Comment on the morphology of the erythrocytes.
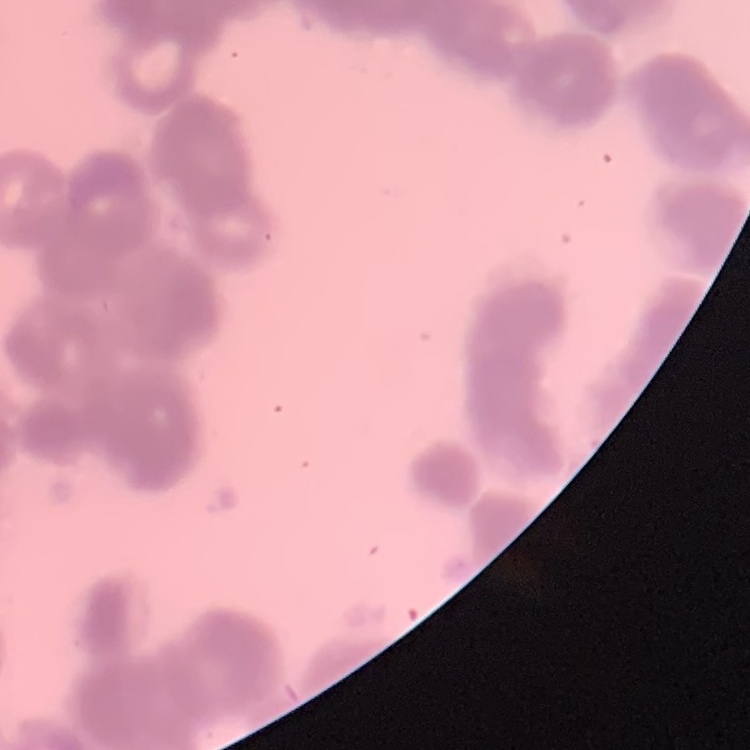

They show rouleaux formation.

preparation = thin blood film
image type = one tile cut from a larger photomicrograph
stain = Field's or Giemsa